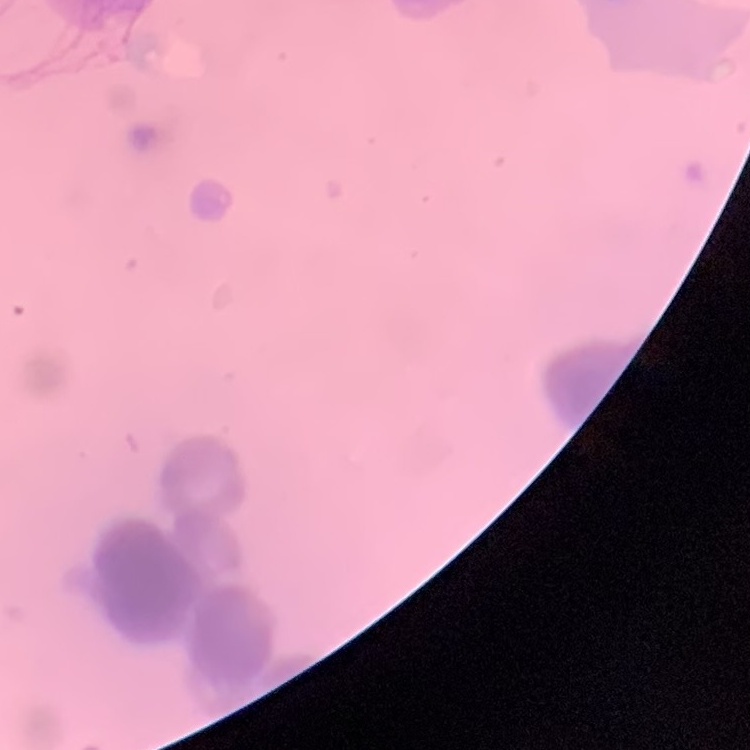 The red blood cells exhibit rouleaux formation. Thin blood film. One tile cut from a larger photomicrograph. Stained with either Field's or Giemsa.